State the blood parasite species.
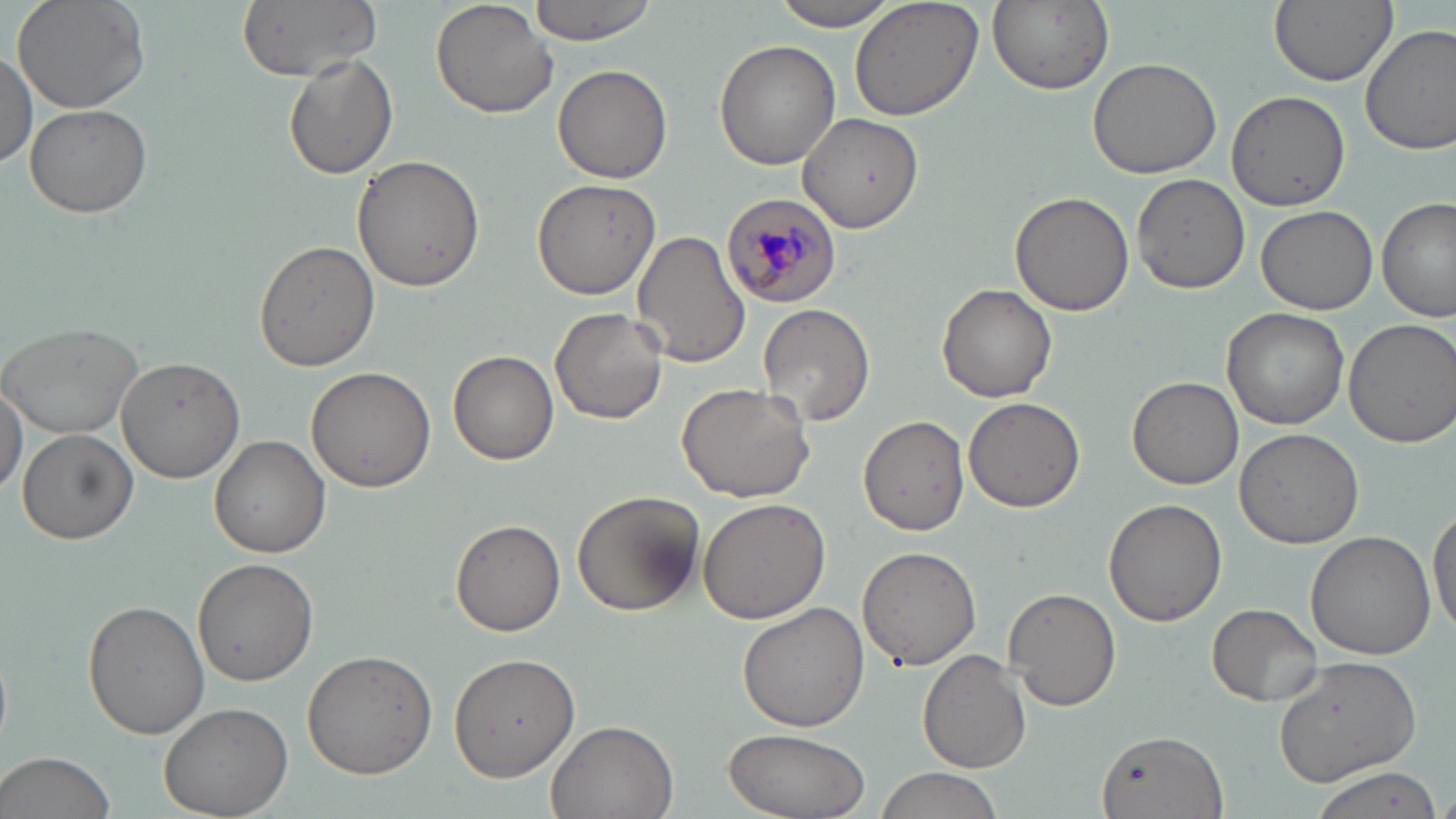

Plasmodium malariae.

preparation: thin blood smear
plasmodium_malariae_infected_red_blood_cell_locations: 'approximate bounding boxes as (x1, y1, x2, y2) in pixels: (720, 194, 845, 307)'
magnification: 1000x
image_size: 1456×819 pixels
uninfected_red_blood_cell_locations: 'approximate bounding boxes as (x1, y1, x2, y2) in pixels: (13, 0, 151, 114), (237, 0, 385, 80), (431, 0, 557, 119), (529, 0, 659, 44), (771, 0, 907, 29), (847, 0, 986, 122), (986, 0, 1115, 94), (1269, 0, 1396, 88), (1361, 25, 1456, 154), (713, 39, 841, 172), (0, 51, 37, 169), (283, 54, 398, 181), (1086, 56, 1224, 179), (552, 64, 674, 183), (1227, 88, 1351, 213), (25, 103, 152, 217), (796, 111, 925, 232), (351, 154, 485, 293), (1132, 175, 1249, 294), (530, 176, 661, 298), (1009, 190, 1133, 319), (1377, 196, 1454, 323), (1255, 205, 1377, 316), (630, 233, 750, 369), (254, 241, 379, 372), (936, 283, 1057, 401), (757, 303, 873, 428), (550, 306, 667, 424), (1221, 306, 1350, 429), (0, 319, 147, 438), (1341, 319, 1452, 448), (447, 350, 558, 466), (115, 355, 245, 483), (306, 366, 438, 495), (1128, 375, 1245, 491), (0, 377, 26, 499), (676, 381, 816, 502), (962, 397, 1085, 513), (858, 416, 970, 535), (17, 428, 138, 544), (1233, 428, 1364, 549), (209, 434, 330, 558), (571, 491, 704, 617), (699, 496, 832, 624), (1104, 498, 1228, 628), (1428, 502, 1456, 634), (452, 519, 566, 636), (1306, 532, 1437, 660), (856, 545, 982, 670), (192, 558, 320, 687), (1004, 588, 1123, 712), (84, 598, 211, 740), (737, 602, 873, 732), (1207, 603, 1322, 706), (449, 648, 580, 781), (302, 649, 437, 779), (918, 650, 1032, 772), (1272, 652, 1423, 786), (159, 703, 292, 818), (546, 719, 678, 819), (720, 728, 872, 819), (1097, 728, 1230, 819), (0, 751, 118, 819), (1305, 766, 1445, 819), (875, 768, 1003, 819)'
field_of_view: one of a larger specimen
stain: May-Grünwald-Giemsa
modality: light microscopy